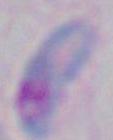

Summary:
  - Modality: photomicrograph
  - Identification: Toxoplasma gondii
  - Magnification: 1000x